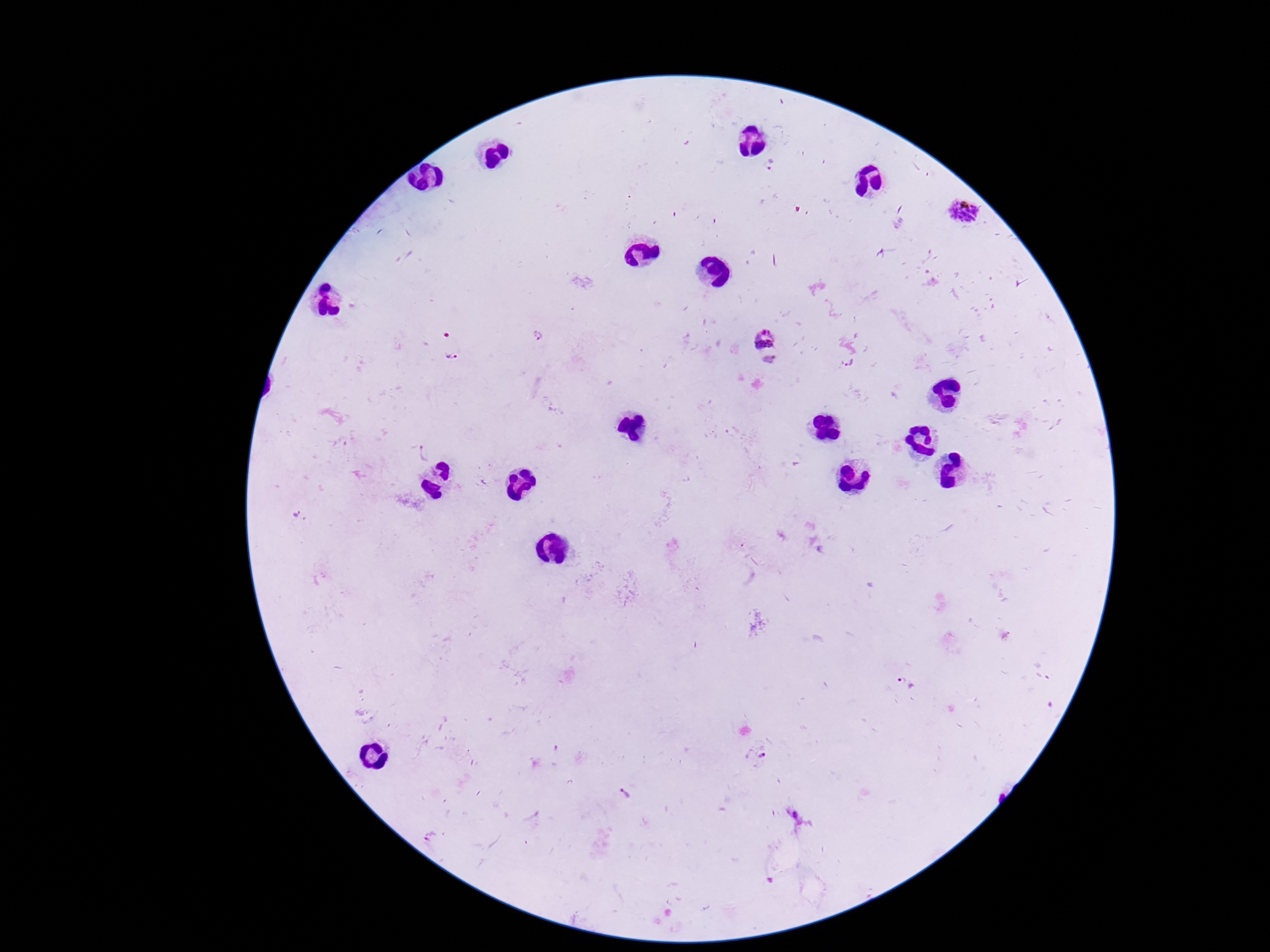

stain = Giemsa
preparation = thick blood film
capture = smartphone camera through the microscope eyepiece
magnification = 100x
patient malaria status = infected
Plasmodium parasite locations = approximate centers as [x, y] in pixels: [769, 162], [963, 210], [539, 336], [763, 339], [452, 354], [770, 361], [850, 363], [423, 451], [906, 684], [759, 756], [626, 795], [796, 817]
field of view = one from this slide
image size = 1270×952 pixels